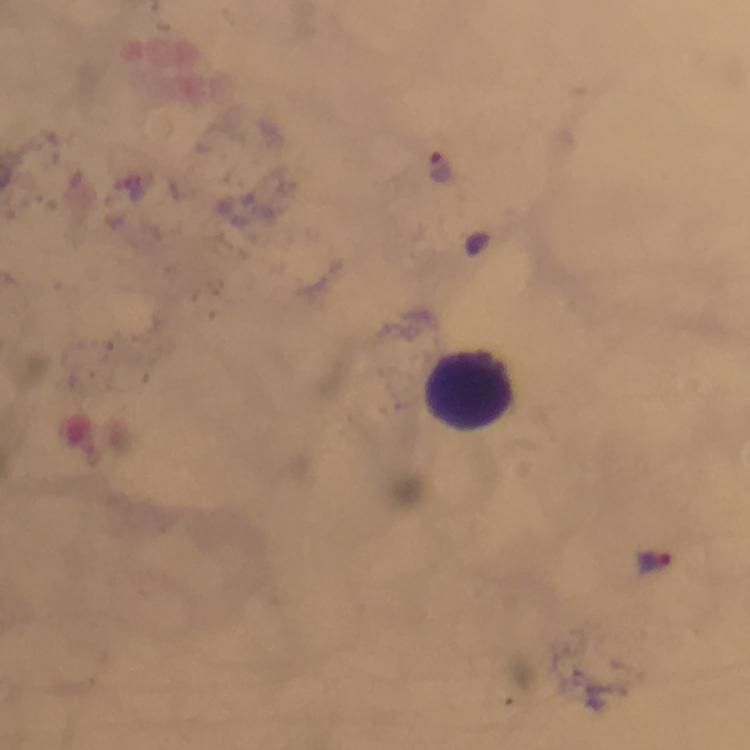

Approximate centers as (x, y) in pixels.
Summary:
  - Leukocyte locations: (467, 388)
  - Plasmodium parasite locations: (437, 166), (657, 560)
  - Stain: Giemsa
  - Immersion oil: applied
  - Capture: smartphone photograph through a microscope
  - Preparation: thick blood film
  - Image size: 750×750 pixels
  - Context: from a malaria diagnostic workup
  - Cropped from: a single field of view
  - Magnification: 100x